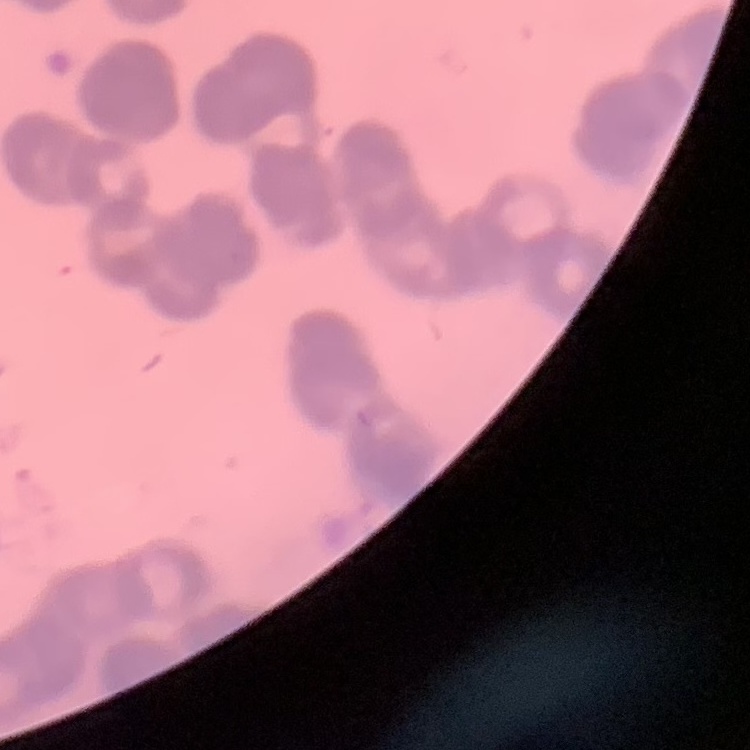 The red blood cells exhibit rouleaux formation. Thin blood smear. Field's or Giemsa stain. Square crop of a larger photomicrograph.